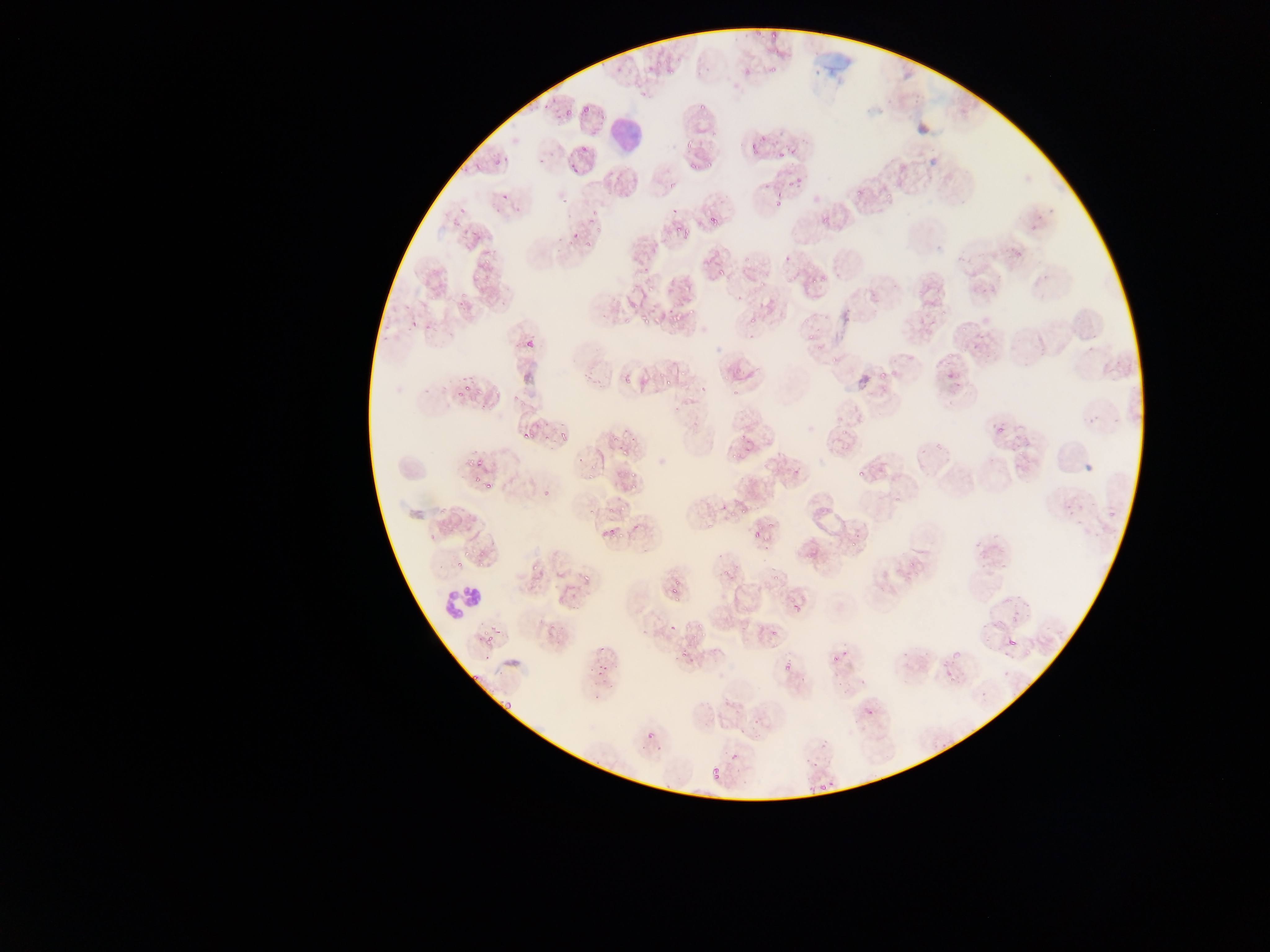
{
  "leukocyte_locations": "approximate bounding boxes as [left, top, right, bottom] in pixels: [612, 115, 643, 154], [443, 586, 488, 618]",
  "field_of_view": "single",
  "country": "Ghana",
  "image_size": "1270×952 pixels",
  "malaria_parasite_locations": "approximate bounding boxes as [left, top, right, bottom] in pixels: [755, 25, 765, 37], [771, 28, 779, 37], [651, 61, 663, 70], [623, 62, 634, 74], [739, 66, 753, 75], [768, 67, 776, 75], [669, 69, 676, 78], [638, 87, 649, 97], [698, 96, 713, 114], [538, 104, 549, 115], [583, 104, 591, 115], [563, 105, 574, 117], [748, 130, 765, 157], [685, 135, 695, 148], [770, 135, 782, 146], [581, 143, 588, 151], [776, 148, 786, 161], [503, 152, 513, 165], [490, 156, 501, 169], [707, 159, 715, 170], [471, 162, 479, 168], [568, 163, 577, 176], [687, 163, 697, 172], [797, 173, 806, 188], [773, 177, 792, 207], [670, 180, 677, 188], [499, 186, 511, 201], [853, 186, 866, 199], [884, 191, 894, 202], [562, 194, 571, 202], [670, 203, 678, 214], [1048, 204, 1059, 215], [457, 206, 466, 212], [589, 209, 599, 223], [703, 212, 716, 225], [820, 217, 828, 224], [1030, 224, 1040, 232], [567, 225, 578, 242], [669, 226, 679, 237], [470, 228, 481, 239], [595, 228, 604, 234], [682, 228, 692, 239], [584, 235, 596, 247], [1013, 241, 1022, 257], [481, 246, 492, 260], [742, 252, 749, 265], [954, 253, 965, 261], [642, 263, 652, 274], [716, 265, 724, 274], [787, 271, 793, 281], [758, 277, 766, 288], [809, 280, 818, 287], [682, 281, 692, 292], [647, 283, 655, 294], [981, 286, 990, 295], [452, 294, 468, 306], [841, 308, 859, 321], [640, 309, 648, 324], [685, 309, 696, 319], [820, 309, 831, 319], [916, 311, 936, 330], [749, 314, 760, 323], [408, 317, 417, 325], [667, 317, 675, 328], [961, 319, 969, 332], [748, 328, 757, 339], [808, 331, 817, 340], [524, 337, 533, 345], [1086, 337, 1100, 358], [971, 342, 980, 353], [816, 344, 825, 352], [942, 346, 953, 364], [829, 355, 838, 365], [583, 366, 596, 381], [879, 366, 886, 384], [680, 369, 687, 377], [655, 370, 663, 380], [623, 375, 628, 383], [952, 377, 963, 390], [455, 383, 473, 398], [699, 385, 707, 391], [732, 387, 738, 396], [989, 416, 1014, 445], [1090, 417, 1103, 424], [557, 426, 572, 439], [840, 426, 850, 436], [522, 430, 532, 438], [737, 431, 748, 442], [611, 433, 619, 444], [629, 433, 639, 442], [1013, 435, 1027, 452], [933, 439, 942, 450], [731, 450, 738, 458], [576, 454, 585, 463], [467, 456, 476, 466], [791, 462, 803, 476], [855, 471, 865, 479], [588, 472, 596, 478], [473, 475, 483, 484], [486, 483, 491, 493], [540, 483, 555, 496], [895, 490, 903, 501], [719, 499, 729, 511], [1061, 500, 1075, 515], [618, 505, 629, 514], [1107, 505, 1117, 518], [589, 510, 597, 517], [630, 515, 647, 532], [766, 520, 773, 529], [607, 528, 617, 539], [755, 530, 762, 539], [427, 534, 435, 540], [761, 539, 771, 554], [972, 539, 982, 552], [480, 549, 487, 560], [907, 556, 916, 567], [456, 558, 463, 568], [979, 558, 991, 569], [532, 563, 540, 573], [721, 568, 730, 576], [772, 572, 780, 583], [582, 575, 588, 583], [669, 583, 678, 595], [672, 597, 678, 605], [788, 597, 798, 612], [1012, 610, 1019, 621], [994, 619, 1005, 627], [545, 620, 560, 637], [981, 620, 989, 633], [667, 622, 675, 632], [770, 626, 777, 637], [484, 631, 493, 644], [982, 633, 993, 646], [1003, 633, 1022, 654], [599, 644, 605, 652], [840, 644, 852, 656], [678, 648, 686, 662], [483, 649, 491, 661], [897, 652, 909, 657], [780, 660, 792, 672], [593, 661, 610, 677], [944, 663, 966, 683], [834, 681, 847, 692], [980, 682, 993, 695], [499, 703, 510, 711], [859, 703, 880, 724], [646, 730, 658, 744], [728, 740, 744, 761], [806, 758, 823, 771], [703, 762, 720, 776], [832, 775, 842, 792], [816, 778, 827, 793], [804, 785, 815, 795] | approximate [x, y] pixel centers of objects too small to bound: [776, 51], [455, 221], [737, 297], [429, 327], [950, 375], [665, 382], [546, 436], [624, 454], [633, 475], [632, 488], [610, 510], [743, 511], [621, 536], [852, 544], [464, 553], [481, 565], [1005, 566], [699, 628], [833, 661], [473, 676], [862, 682], [597, 696]",
  "capture": "mobile-phone photograph through a microscope",
  "preparation": "thin blood film"
}